Point out each leukocyte.
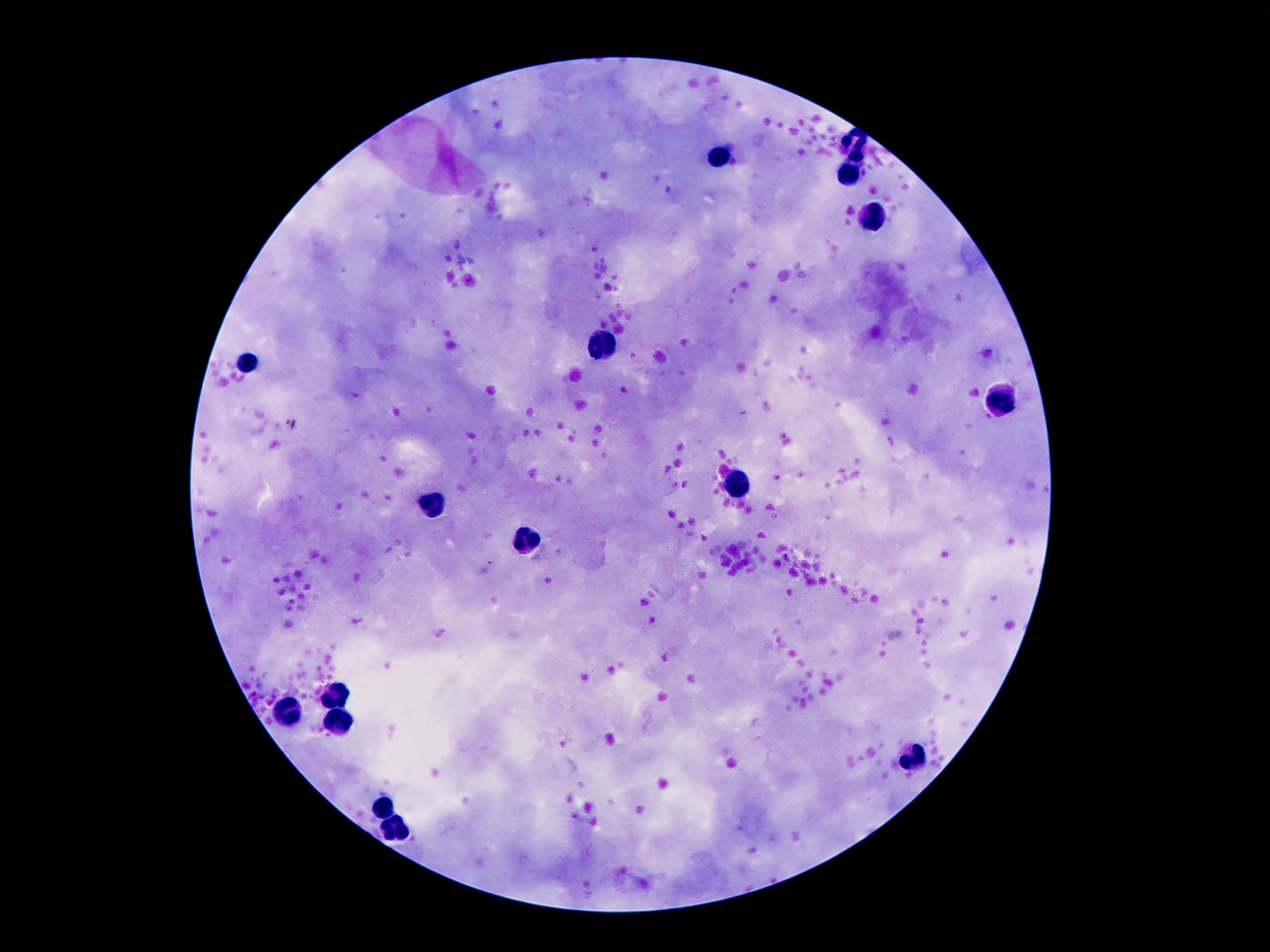
Approximate centers as {x, y} in pixels.
Leukocytes: {858, 141}, {722, 158}, {849, 169}, {870, 215}, {604, 346}, {250, 360}, {1004, 398}, {738, 483}, {434, 508}, {525, 541}, {336, 695}, {288, 710}, {343, 720}, {911, 759}, {384, 809}, {393, 834}.

field of view = single
patient malaria status = uninfected
magnification = 100x
capture = smartphone camera through the microscope eyepiece
stain = Giemsa
image size = 1270×952 pixels
preparation = thick blood film